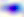 Toxoplasma gondii is shown. 400x magnification. Micrograph.